Mark where platelets are.
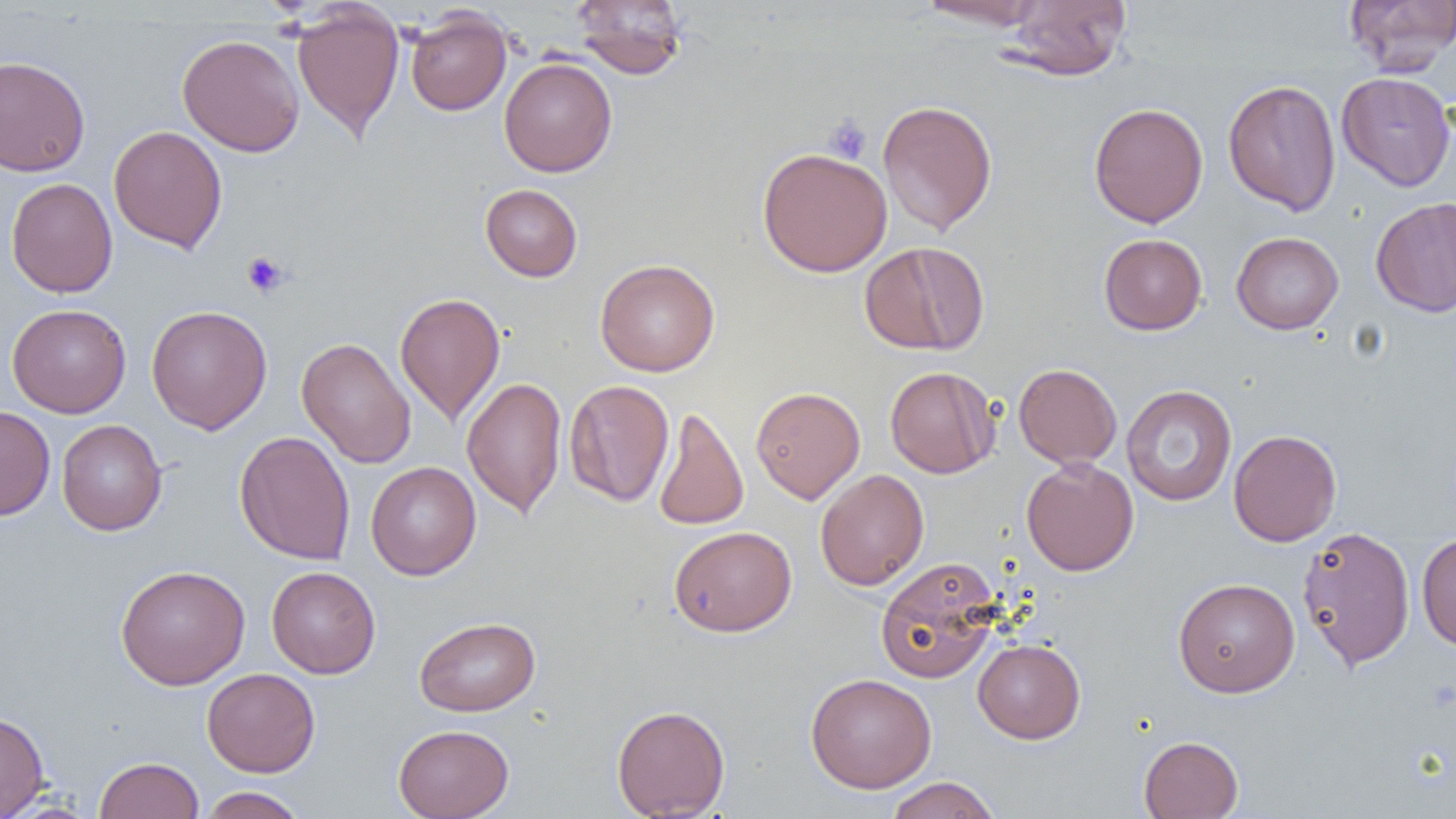
Approximate bounding boxes as (x1, y1, x2, y2) in pixels.
Platelets: (824, 115, 872, 164), (241, 251, 290, 298).

slide-level diagnosis = no evidence of blood parasites
preparation = thin blood film
uninfected red blood cell locations = approximate bounding boxes as (x1, y1, x2, y2) in pixels: (571, 0, 688, 80), (915, 0, 1049, 30), (1001, 0, 1132, 81), (1345, 0, 1456, 75), (291, 4, 404, 141), (405, 7, 512, 116), (177, 34, 305, 157), (0, 55, 91, 177), (499, 56, 617, 177), (1336, 72, 1456, 192), (1223, 79, 1341, 216), (878, 99, 998, 235), (1089, 101, 1208, 228), (109, 125, 227, 253), (756, 147, 892, 277), (5, 177, 118, 298), (480, 184, 583, 282), (1370, 197, 1456, 317), (1231, 231, 1344, 334), (1099, 234, 1207, 335), (860, 241, 989, 356), (595, 259, 720, 377), (394, 292, 506, 425), (7, 303, 131, 418), (146, 304, 272, 434), (297, 337, 416, 469), (1013, 363, 1122, 468), (885, 366, 999, 479), (461, 376, 567, 518), (564, 379, 674, 506), (1121, 385, 1237, 506), (750, 386, 865, 503), (0, 406, 56, 521), (654, 407, 749, 530), (57, 419, 167, 535), (1228, 429, 1342, 547), (234, 430, 355, 565), (1021, 457, 1138, 576), (366, 461, 481, 580), (815, 469, 929, 590), (1296, 525, 1415, 672), (669, 526, 797, 637), (1416, 532, 1456, 652), (875, 556, 1003, 684), (116, 564, 251, 690), (267, 566, 380, 679), (1173, 577, 1300, 697), (414, 616, 540, 716), (973, 639, 1086, 743), (202, 667, 320, 777), (805, 672, 937, 793), (612, 703, 730, 818), (0, 711, 50, 818), (393, 724, 514, 819), (1138, 735, 1243, 818), (94, 756, 204, 818), (884, 777, 1002, 819), (198, 786, 307, 818)
magnification = 1000x
field of view = single
modality = light microscopy
image size = 1456×819 pixels